State which parasite is depicted.
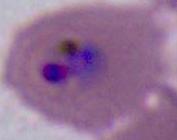
This is Plasmodium.

magnification = 400x or 1000x
modality = photomicrograph